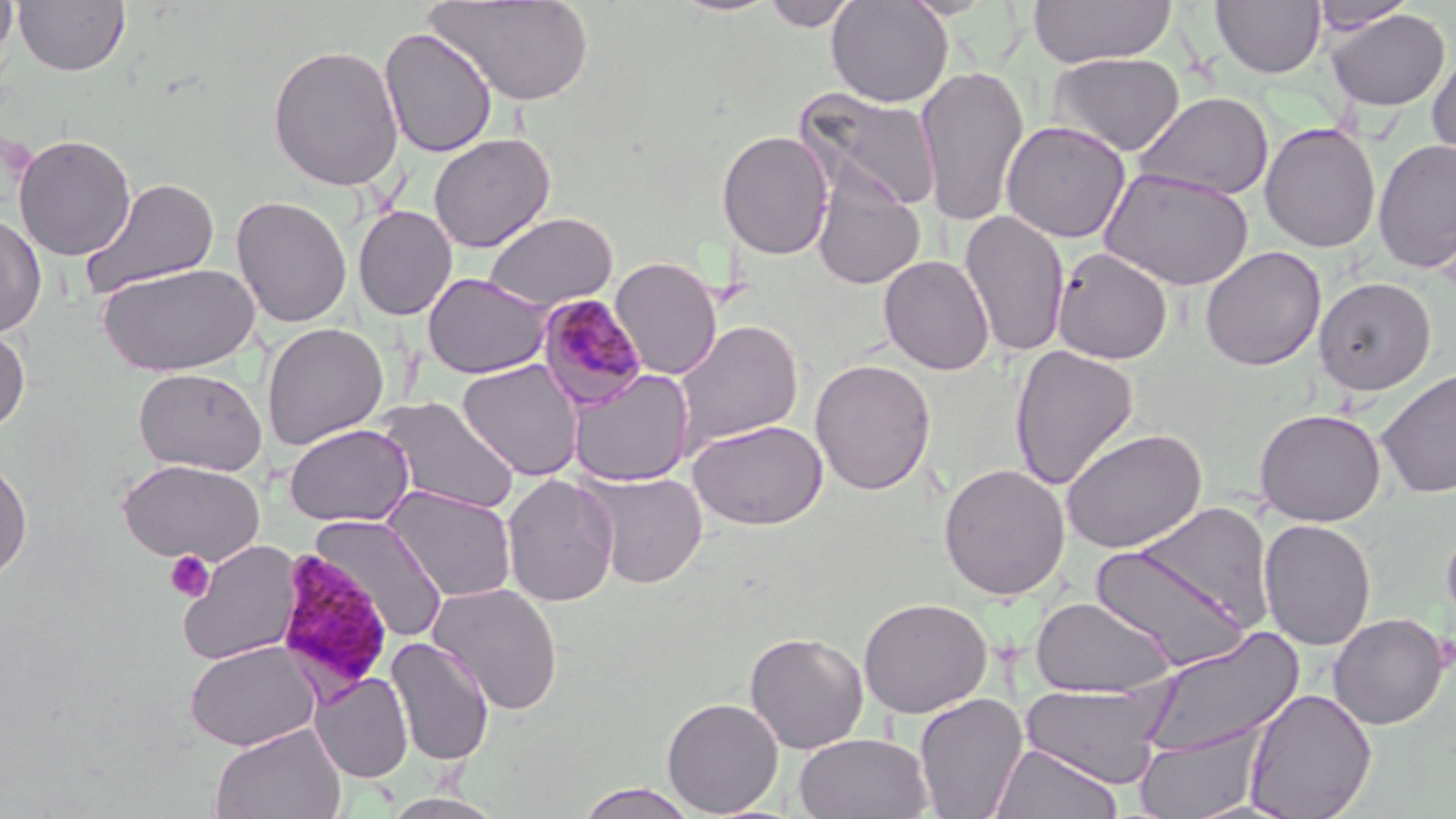
Summary:
  - Coordinate format: approximate bounding boxes as named x1/y1/x2/y2 corners in pixels
  - Plasmodium malariae-infected red blood cell locations: (x1=535, y1=293, x2=648, y2=412), (x1=273, y1=548, x2=395, y2=696)
  - Platelet locations: (x1=165, y1=550, x2=215, y2=602)
  - Uninfected red blood cell locations: (x1=0, y1=0, x2=18, y2=62), (x1=14, y1=0, x2=130, y2=77), (x1=424, y1=0, x2=596, y2=106), (x1=826, y1=0, x2=953, y2=108), (x1=898, y1=0, x2=999, y2=19), (x1=1028, y1=0, x2=1177, y2=67), (x1=760, y1=1, x2=860, y2=31), (x1=1212, y1=1, x2=1326, y2=79), (x1=1310, y1=1, x2=1417, y2=34), (x1=1325, y1=8, x2=1451, y2=111), (x1=379, y1=27, x2=498, y2=158), (x1=267, y1=43, x2=405, y2=192), (x1=1428, y1=49, x2=1456, y2=166), (x1=1048, y1=52, x2=1186, y2=157), (x1=916, y1=63, x2=1030, y2=227), (x1=798, y1=88, x2=943, y2=215), (x1=1133, y1=92, x2=1275, y2=201), (x1=1000, y1=120, x2=1131, y2=243), (x1=1259, y1=122, x2=1381, y2=253), (x1=716, y1=129, x2=835, y2=260), (x1=13, y1=133, x2=137, y2=261), (x1=428, y1=133, x2=556, y2=252), (x1=1372, y1=139, x2=1456, y2=273), (x1=1099, y1=167, x2=1254, y2=290), (x1=81, y1=178, x2=221, y2=297), (x1=811, y1=180, x2=926, y2=290), (x1=231, y1=195, x2=352, y2=328), (x1=353, y1=206, x2=457, y2=321), (x1=959, y1=209, x2=1070, y2=358), (x1=484, y1=212, x2=619, y2=311), (x1=0, y1=213, x2=46, y2=337), (x1=1200, y1=246, x2=1326, y2=372), (x1=1052, y1=247, x2=1173, y2=364), (x1=878, y1=255, x2=995, y2=376), (x1=610, y1=257, x2=724, y2=379), (x1=97, y1=262, x2=260, y2=376), (x1=422, y1=272, x2=552, y2=379), (x1=1314, y1=277, x2=1436, y2=396), (x1=673, y1=320, x2=803, y2=452), (x1=262, y1=323, x2=389, y2=450), (x1=0, y1=325, x2=31, y2=432), (x1=1009, y1=343, x2=1139, y2=491), (x1=810, y1=358, x2=936, y2=495), (x1=458, y1=359, x2=583, y2=481), (x1=133, y1=367, x2=267, y2=475), (x1=1376, y1=367, x2=1456, y2=499), (x1=568, y1=368, x2=695, y2=487), (x1=375, y1=397, x2=520, y2=515), (x1=1254, y1=407, x2=1387, y2=526), (x1=689, y1=419, x2=828, y2=530), (x1=284, y1=423, x2=414, y2=527), (x1=1060, y1=427, x2=1207, y2=554), (x1=0, y1=458, x2=32, y2=583), (x1=117, y1=458, x2=264, y2=565), (x1=937, y1=463, x2=1070, y2=600), (x1=582, y1=470, x2=708, y2=589), (x1=502, y1=473, x2=620, y2=607), (x1=384, y1=486, x2=517, y2=602), (x1=310, y1=514, x2=449, y2=643), (x1=1258, y1=518, x2=1376, y2=651), (x1=1440, y1=519, x2=1456, y2=639), (x1=177, y1=540, x2=303, y2=665), (x1=1089, y1=541, x2=1255, y2=671), (x1=427, y1=582, x2=564, y2=715), (x1=1030, y1=595, x2=1176, y2=699), (x1=858, y1=597, x2=992, y2=718), (x1=1328, y1=613, x2=1450, y2=729), (x1=1138, y1=627, x2=1306, y2=761), (x1=744, y1=631, x2=869, y2=754), (x1=386, y1=637, x2=494, y2=766), (x1=184, y1=640, x2=321, y2=751), (x1=311, y1=672, x2=413, y2=783), (x1=1020, y1=682, x2=1170, y2=788), (x1=1243, y1=688, x2=1378, y2=818), (x1=913, y1=692, x2=1029, y2=818), (x1=662, y1=697, x2=783, y2=817), (x1=209, y1=724, x2=346, y2=819), (x1=1135, y1=726, x2=1263, y2=818), (x1=794, y1=732, x2=934, y2=818), (x1=990, y1=742, x2=1123, y2=819), (x1=574, y1=783, x2=700, y2=819), (x1=382, y1=792, x2=506, y2=819)
  - Slide-level diagnosis: Plasmodium malariae
  - Stain: May-Grünwald-Giemsa
  - Preparation: thin blood smear
  - Magnification: 1000x
  - Modality: optical microscopy
  - Image size: 1456×819 pixels
  - Field of view: one of a larger specimen